Draw a bounding box around every leukocyte (white blood cell).
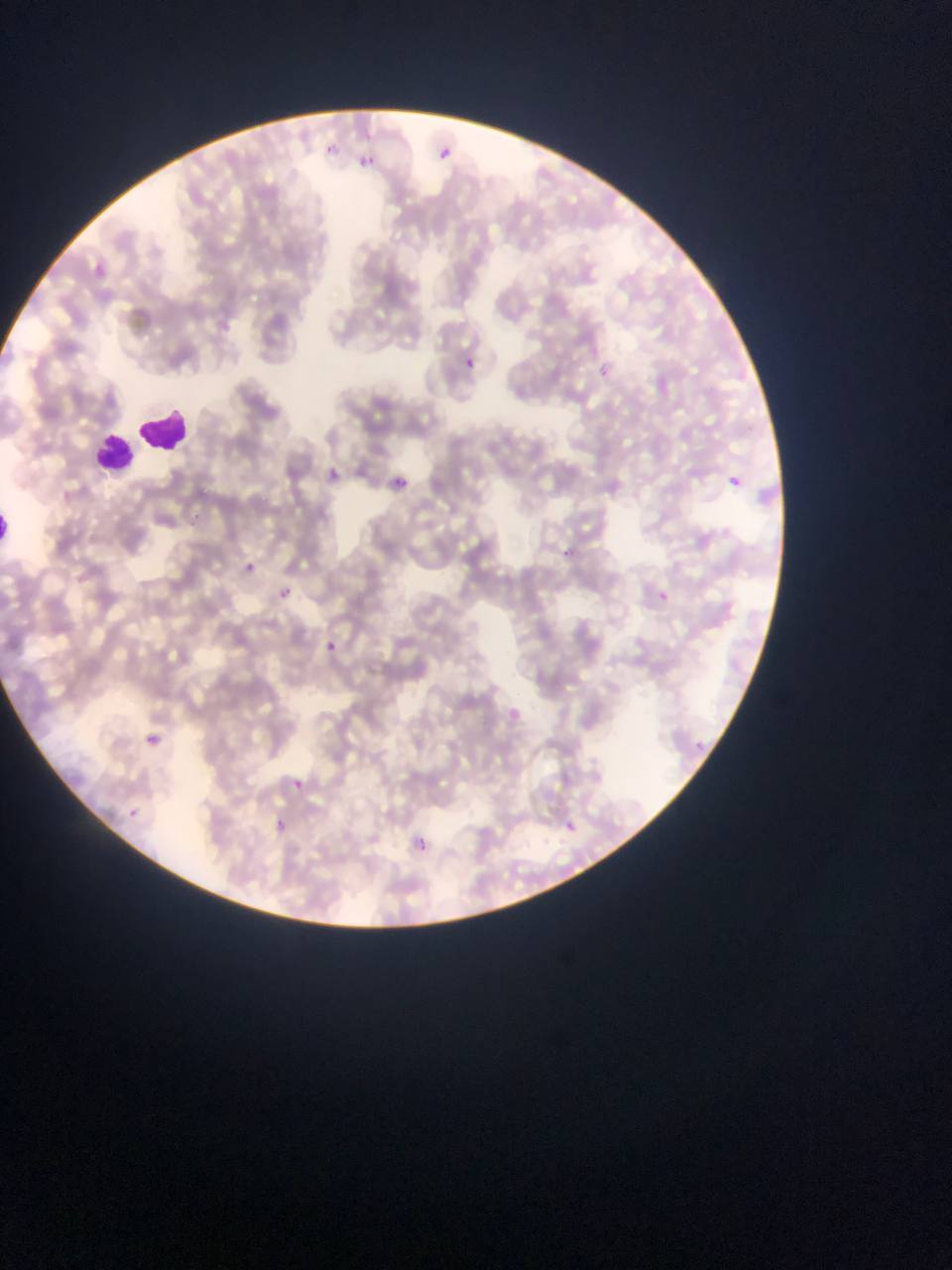
Approximate bounding boxes as (left, top, right, bottom) in pixels.
Leukocytes: (135, 403, 190, 458), (88, 427, 141, 476), (0, 513, 18, 544).

Malaria parasite locations: (458, 352, 481, 374), (320, 461, 348, 489), (383, 471, 415, 497), (720, 472, 745, 494), (551, 543, 581, 569), (237, 557, 259, 578), (273, 584, 294, 603), (651, 587, 673, 606), (317, 634, 343, 660), (139, 729, 162, 752), (284, 771, 312, 796), (121, 804, 143, 824), (555, 816, 580, 839), (268, 819, 292, 839), (407, 830, 438, 859). Sample from Ghana. Photographed through a microscope with a mobile-phone camera. Image is 952×1270 pixels. Thin blood smear. One field of view.